Report the malaria status of this cell.
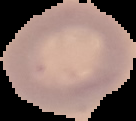

Uninfected.

{
  "image_type": "cell region segmented out of the field of view; surrounding area masked to black",
  "preparation": "thin blood film",
  "image_size": "136×121 pixels"
}